Report the malaria status of this cell.
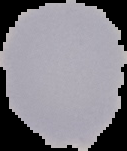

It is uninfected.

preparation = thin blood smear
image size = 127×151 pixels
image type = segmented cell region on a black background